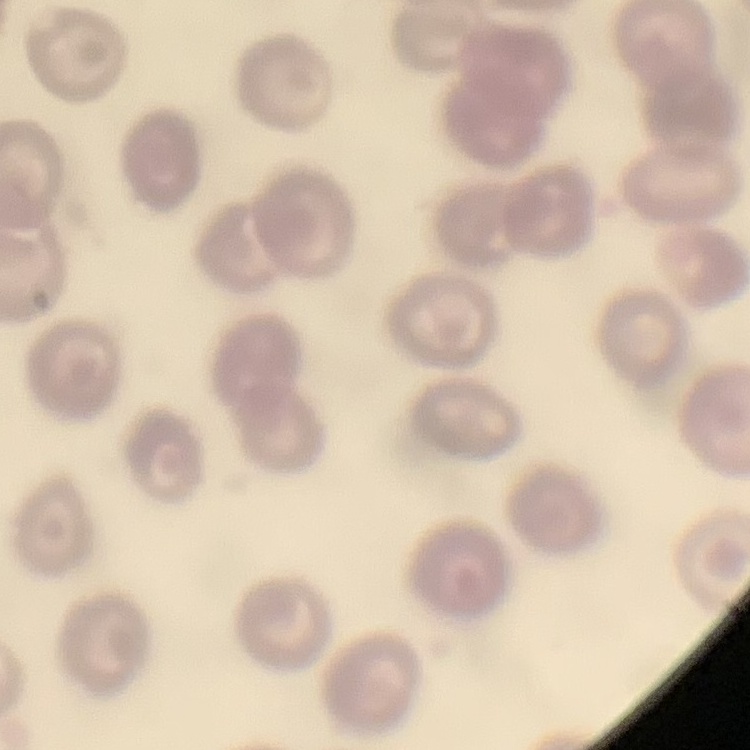

erythrocyte morphology = no rouleaux formation
image type = one tile cut from a larger photomicrograph
stain = Field's or Giemsa
preparation = thin blood film